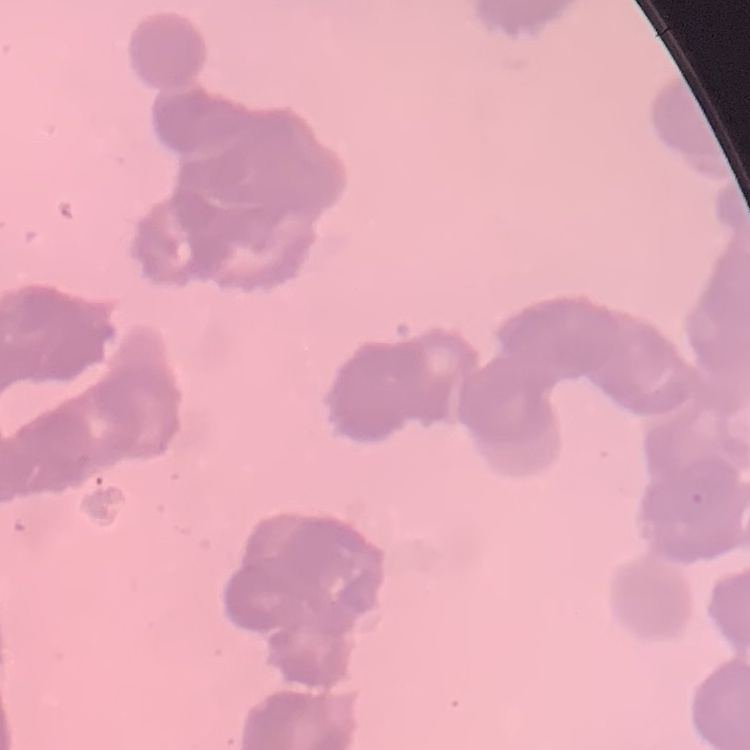
Summary:
  - Erythrocyte morphology: rouleaux formation
  - Preparation: thin peripheral smear
  - Stain: Field's or Giemsa
  - Image type: square crop of a larger photomicrograph